Describe the morphology of the red blood cells.
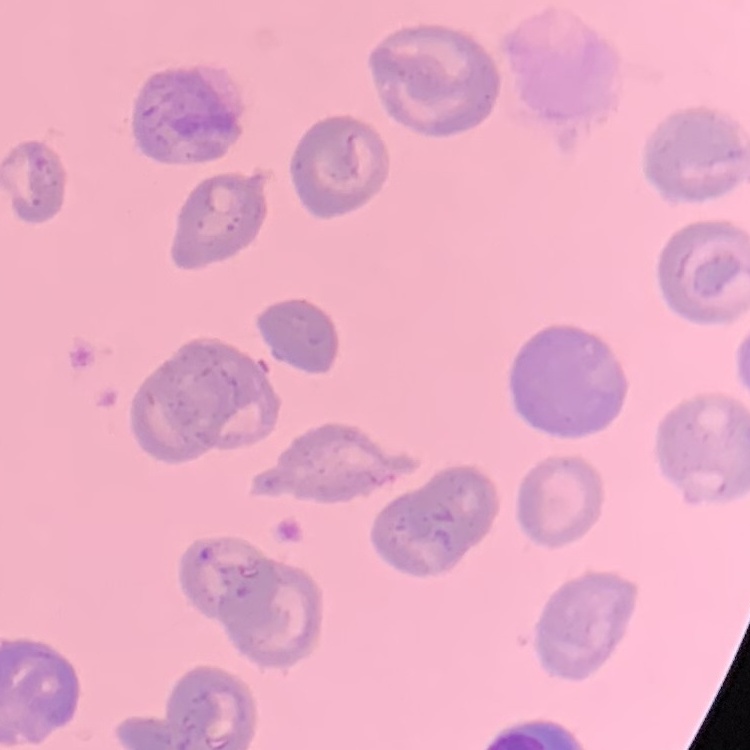

They show no rouleaux formation.

Thin peripheral smear. Stained with either Field's or Giemsa. Square crop of a larger photomicrograph.